Locate every Plasmodium falciparum-infected red blood cell.
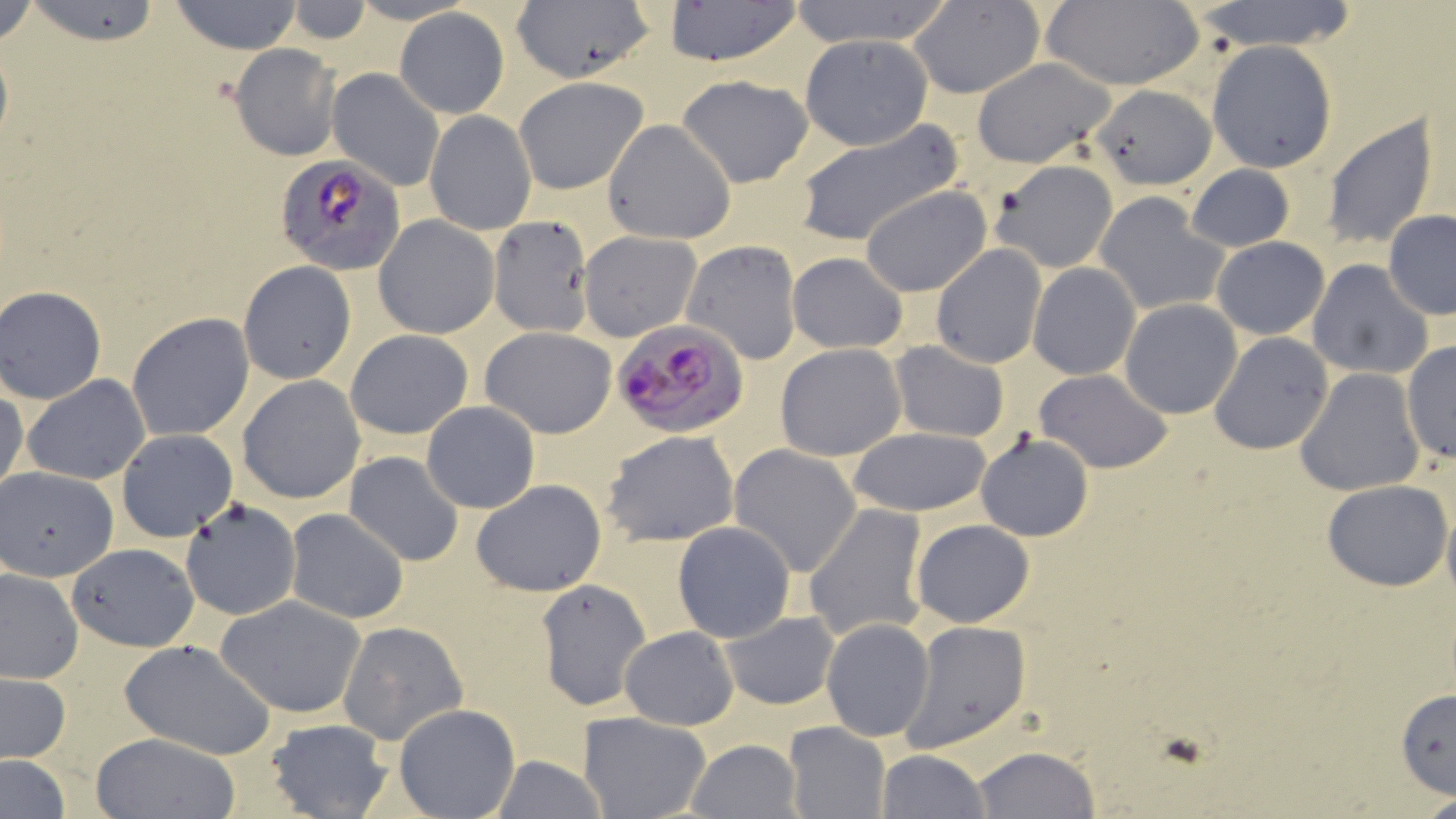

Approximate bounding boxes as (x1, y1, x2, y2) in pixels.
Plasmodium falciparum-infected red blood cells: (275, 155, 406, 275), (614, 321, 748, 438).

Summary:
  - Uninfected red blood cell locations: (0, 0, 39, 49), (24, 0, 166, 46), (168, 0, 306, 54), (786, 0, 955, 49), (906, 0, 1045, 97), (282, 1, 375, 45), (664, 1, 804, 66), (1191, 1, 1360, 53), (510, 2, 657, 83), (1037, 3, 1207, 90), (395, 8, 509, 119), (799, 34, 934, 150), (1206, 40, 1336, 172), (229, 45, 341, 161), (969, 56, 1119, 169), (326, 67, 445, 191), (676, 73, 814, 187), (514, 76, 648, 195), (1089, 83, 1219, 190), (425, 110, 535, 235), (1321, 113, 1439, 250), (602, 119, 736, 244), (793, 119, 959, 247), (988, 159, 1120, 273), (1185, 163, 1296, 253), (861, 185, 992, 297), (1093, 190, 1231, 316), (1383, 211, 1456, 321), (374, 216, 500, 339), (488, 217, 593, 336), (578, 230, 702, 342), (1212, 237, 1329, 340), (683, 240, 802, 364), (931, 244, 1048, 368), (786, 253, 908, 352), (1308, 260, 1434, 381), (238, 261, 356, 385), (1028, 262, 1143, 380), (0, 285, 110, 404), (1119, 299, 1243, 418), (126, 311, 255, 442), (480, 326, 617, 438), (345, 328, 473, 440), (1208, 332, 1334, 456), (1401, 340, 1455, 466), (890, 341, 1009, 443), (775, 343, 907, 462), (1035, 369, 1172, 474), (1296, 369, 1426, 497), (23, 375, 151, 485), (237, 376, 365, 505), (0, 384, 27, 505), (421, 400, 540, 514), (408, 407, 563, 586), (848, 427, 991, 518), (115, 429, 238, 542), (602, 430, 740, 547), (975, 432, 1093, 541), (729, 444, 864, 577), (345, 451, 464, 566), (0, 467, 119, 580), (1321, 478, 1454, 590), (470, 480, 606, 598), (180, 497, 302, 621), (804, 504, 929, 640), (285, 508, 410, 624), (910, 519, 1035, 628), (672, 520, 796, 643), (67, 541, 199, 650), (0, 567, 82, 683), (535, 578, 650, 712), (217, 594, 367, 718), (717, 610, 841, 710), (821, 618, 936, 742), (900, 618, 1030, 752), (338, 621, 468, 745), (620, 626, 738, 730), (118, 639, 277, 759), (1, 672, 72, 763), (1395, 689, 1456, 799), (392, 704, 520, 818), (578, 712, 712, 819), (262, 718, 394, 819), (784, 722, 890, 819), (90, 732, 240, 818), (686, 739, 802, 819), (972, 746, 1100, 819), (876, 749, 990, 818), (488, 755, 609, 818), (1, 759, 71, 816), (1413, 792, 1456, 819)
  - Slide-level diagnosis: Plasmodium falciparum
  - Preparation: thin blood film
  - Field of view: single
  - Stain: May-Grünwald-Giemsa
  - Magnification: 1000x
  - Modality: light microscopy
  - Image size: 1456×819 pixels